Locate the red blood cells and classify each one as P. falciparum-infected, uninfected, or of indeterminate infection status.
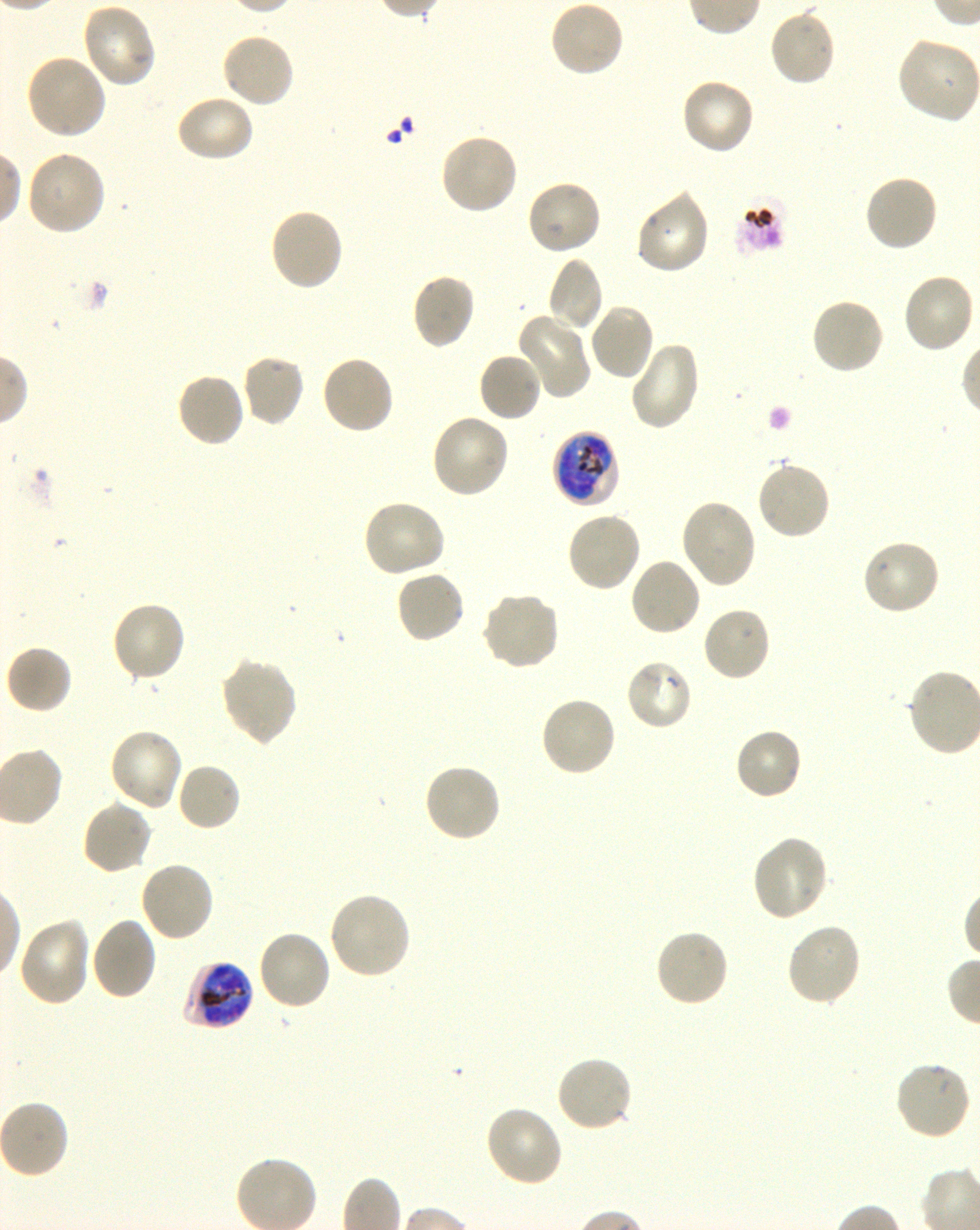
Approximate bounding boxes as [x1, y1, x2, y2] in pixels. Not every red blood cell is marked. A life-cycle stage — or a range of stages, where the recorded stages span more than one — follows each staged infected red blood cell.
Infected red blood cells: [551, 429, 621, 508] late trophozoite to early schizont; [182, 958, 256, 1032] late trophozoite to late schizont.
Uninfected red blood cells: [548, 0, 625, 80], [81, 3, 158, 88], [768, 7, 837, 87], [220, 33, 296, 110], [896, 37, 977, 124], [25, 53, 107, 140], [680, 78, 756, 156], [174, 94, 256, 163], [439, 132, 519, 216], [25, 150, 106, 236], [862, 173, 939, 254], [524, 179, 602, 257], [634, 189, 711, 275], [268, 207, 345, 292], [546, 256, 604, 332], [900, 272, 975, 355], [410, 273, 477, 351], [809, 297, 886, 376], [587, 303, 656, 381], [518, 314, 592, 398], [628, 341, 701, 431], [477, 351, 543, 423], [241, 353, 304, 427], [319, 354, 395, 435], [174, 372, 247, 449], [429, 412, 511, 498], [755, 460, 831, 542], [362, 498, 447, 579], [680, 498, 758, 590], [565, 511, 642, 594], [861, 538, 942, 617], [628, 556, 702, 637], [394, 569, 466, 646], [480, 590, 561, 671], [110, 601, 187, 683], [701, 605, 773, 683], [4, 644, 73, 715], [219, 657, 298, 746], [625, 658, 694, 731], [539, 695, 617, 778], [734, 727, 804, 802], [108, 728, 184, 813], [175, 762, 242, 832], [422, 762, 503, 844], [80, 799, 153, 875], [750, 834, 830, 922], [138, 860, 215, 943], [327, 892, 413, 981], [18, 917, 92, 1008], [89, 917, 158, 1001], [784, 922, 862, 1007], [653, 927, 730, 1008], [256, 929, 332, 1011], [554, 1054, 633, 1133], [894, 1061, 972, 1142], [483, 1105, 564, 1188], [233, 1154, 319, 1230].
No red blood cells of indeterminate infection status observed.

{
  "culture": "in-vitro P. falciparum strain 3D7, shaking",
  "field_of_view": "one from this slide",
  "preparation": "thin blood film",
  "stain": "Giemsa",
  "image_size": "980×1230 pixels",
  "donor_blood_group": "O+",
  "objective": "100x, oil immersion, numerical aperture 1.30"
}